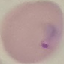 Result: malaria parasites detected. Photographed with a smartphone camera at the microscope eyepiece. Giemsa-stained preparation. Thin smear of blood. Automatically extracted cell patch, resized to 64 × 64 pixels.